Locate and identify every blood parasite.
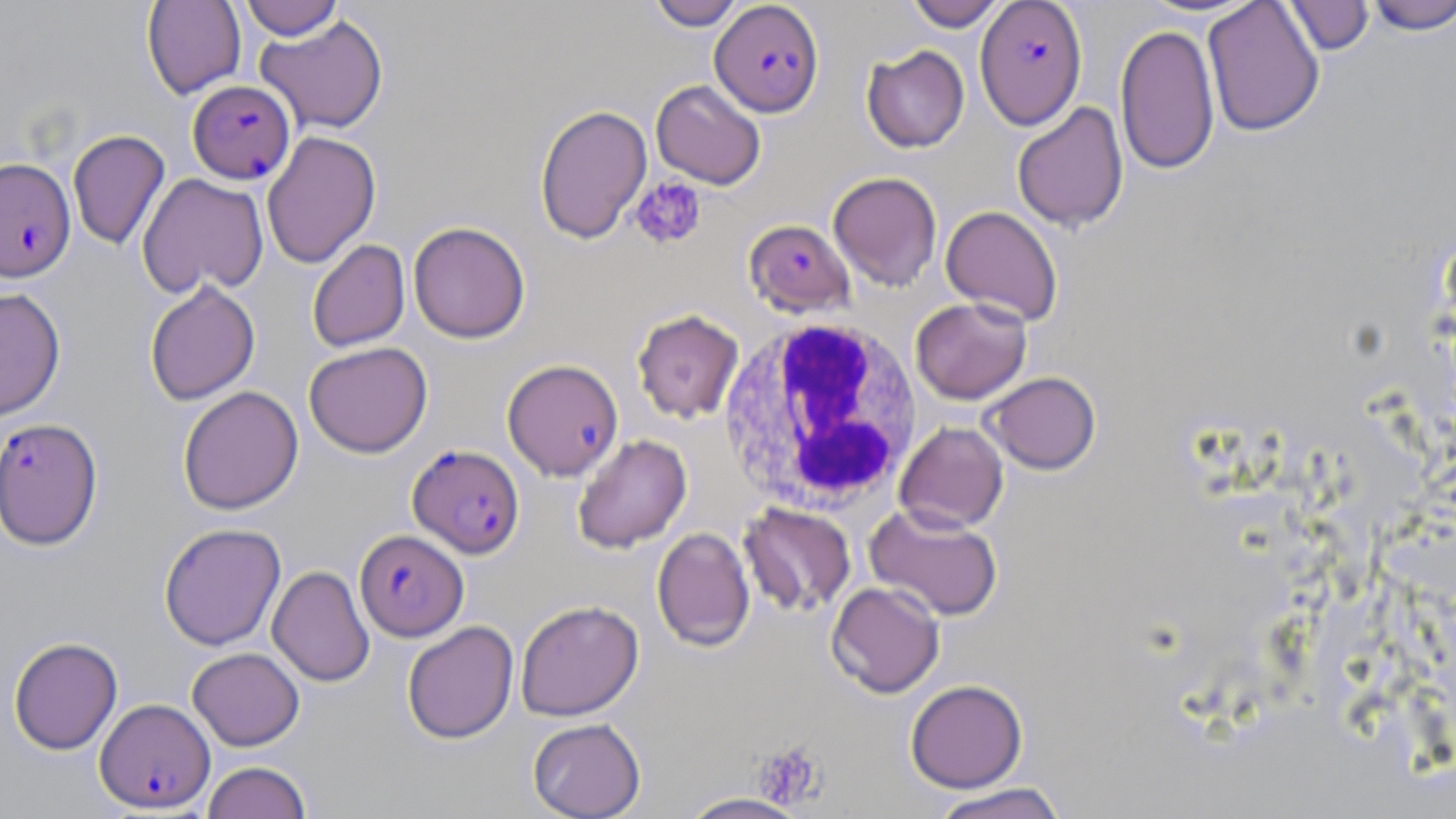
Approximate bounding boxes as (x1,y1)-(x2,y2) corner pairs in pixels.
Plasmodium falciparum-infected red blood cells: (710,0)-(824,117), (975,0)-(1087,129), (188,80)-(295,184), (0,157)-(75,282), (744,219)-(854,316), (502,358)-(623,481), (1,418)-(103,550), (407,444)-(525,559), (354,529)-(469,641), (96,698)-(215,813).
No Plasmodium ovale, Plasmodium malariae, Plasmodium vivax, Babesia divergens, or Trypanosoma brucei observed.

White blood cell locations: (718,318)-(924,514). Platelet locations: (629,177)-(707,251), (753,741)-(827,809). Uninfected red blood cell locations: (141,0)-(246,100), (239,0)-(345,40), (647,0)-(745,30), (903,0)-(1008,30), (1202,0)-(1325,137), (1364,0)-(1456,35), (1281,1)-(1375,56), (254,15)-(389,134), (1115,23)-(1220,176), (861,45)-(969,153), (650,79)-(766,190), (1011,102)-(1129,232), (534,104)-(652,244), (68,129)-(170,251), (261,131)-(381,269), (828,171)-(942,292), (137,173)-(269,298), (940,205)-(1064,326), (407,221)-(531,344), (307,239)-(410,353), (144,280)-(260,406), (0,287)-(66,421), (910,297)-(1032,404), (632,309)-(744,423), (304,342)-(433,458), (984,372)-(1101,475), (178,386)-(304,515), (174,387)-(294,651), (895,421)-(1009,533), (572,433)-(692,554), (739,503)-(856,618), (864,504)-(1003,621), (158,523)-(286,651), (652,527)-(755,652), (267,566)-(374,687), (826,581)-(946,699), (515,600)-(644,721), (402,621)-(518,744), (8,637)-(123,755), (187,647)-(305,750), (905,679)-(1028,793), (527,718)-(646,819), (201,761)-(313,819), (929,782)-(1070,819), (676,792)-(814,819). Slide-level diagnosis: Plasmodium falciparum. Light microscopy. Image is 1456×819 pixels. Thin blood smear. May-Grünwald-Giemsa stain. 1000x magnification. Single field of view.